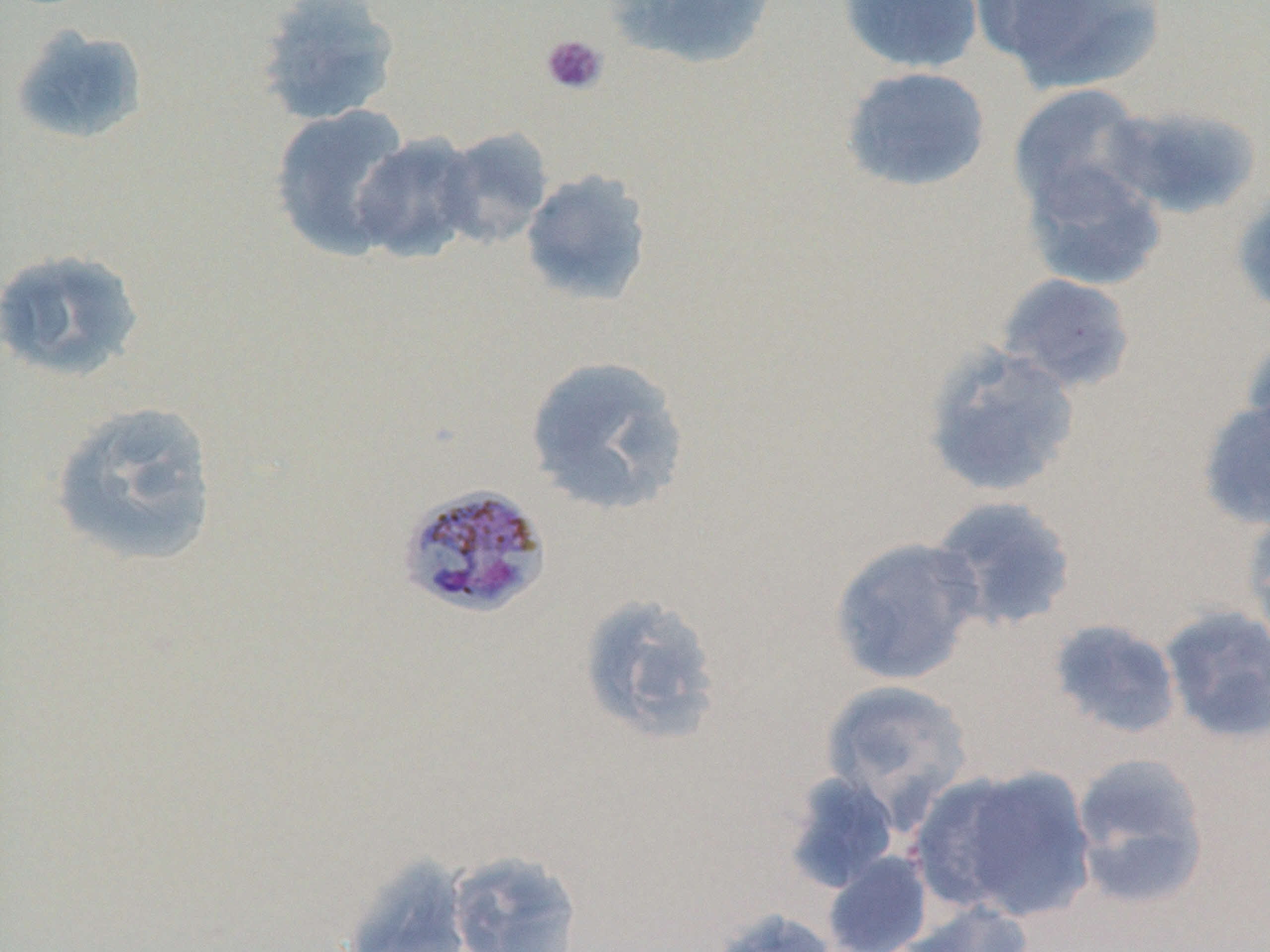

Approximate bounding boxes as named x1/y1/x2/y2 corners in pixels. Uninfected red blood cell locations: (x1=253, y1=0, x2=403, y2=126), (x1=608, y1=0, x2=779, y2=70), (x1=837, y1=0, x2=984, y2=74), (x1=975, y1=0, x2=1165, y2=95), (x1=9, y1=24, x2=149, y2=147), (x1=839, y1=65, x2=992, y2=193), (x1=1007, y1=83, x2=1152, y2=220), (x1=269, y1=103, x2=415, y2=261), (x1=1100, y1=103, x2=1263, y2=219), (x1=436, y1=126, x2=554, y2=249), (x1=350, y1=131, x2=482, y2=264), (x1=1019, y1=158, x2=1167, y2=292), (x1=519, y1=169, x2=654, y2=308), (x1=1232, y1=185, x2=1270, y2=318), (x1=0, y1=248, x2=147, y2=383), (x1=995, y1=273, x2=1137, y2=394), (x1=1239, y1=327, x2=1270, y2=455), (x1=920, y1=342, x2=1082, y2=499), (x1=522, y1=354, x2=691, y2=516), (x1=47, y1=399, x2=221, y2=570), (x1=1196, y1=400, x2=1270, y2=532), (x1=927, y1=494, x2=1079, y2=634), (x1=1240, y1=508, x2=1270, y2=656), (x1=827, y1=535, x2=985, y2=687), (x1=576, y1=592, x2=725, y2=746), (x1=1158, y1=605, x2=1270, y2=744), (x1=1046, y1=618, x2=1183, y2=740), (x1=820, y1=680, x2=975, y2=823), (x1=1069, y1=752, x2=1213, y2=910), (x1=912, y1=763, x2=1101, y2=925), (x1=782, y1=771, x2=901, y2=894), (x1=446, y1=850, x2=584, y2=951), (x1=822, y1=851, x2=934, y2=952), (x1=342, y1=854, x2=473, y2=952), (x1=895, y1=900, x2=1035, y2=952), (x1=710, y1=906, x2=841, y2=952). Plasmodium malariae-infected red blood cell locations: (x1=395, y1=482, x2=553, y2=620). Platelet locations: (x1=540, y1=34, x2=608, y2=96). Slide-level diagnosis: Plasmodium malariae. 1000x magnification. Thin blood film. May-Grünwald-Giemsa stain. Light microscopy. One field of a larger specimen. Image is 1270×952 pixels.